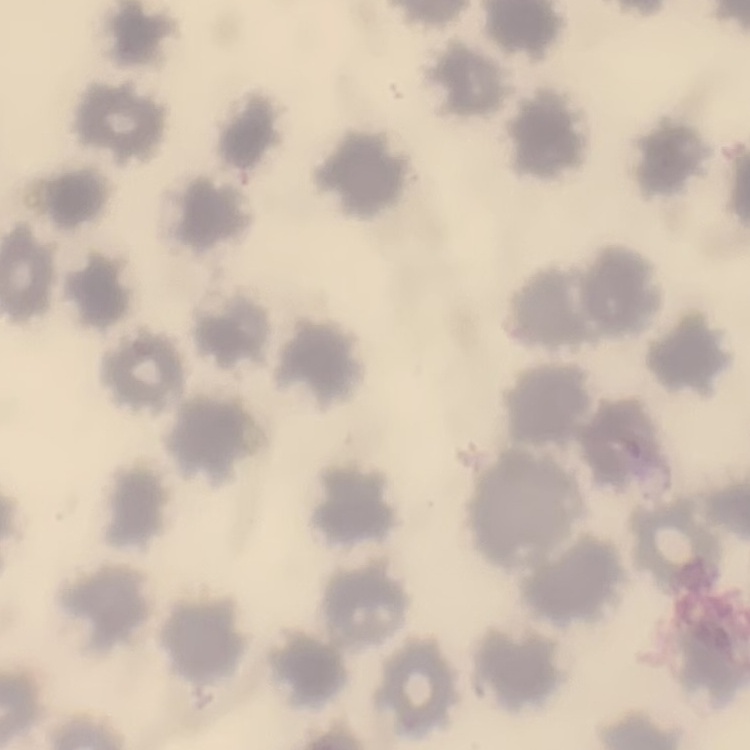

The erythrocytes show no rouleaux formation. Thin blood film. Square crop of a larger photomicrograph. Field's or Giemsa stain.